Assess this cell for malaria.
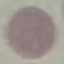
It is uninfected.

capture: smartphone through the microscope eyepiece
stain: Giemsa
image_type: automatically extracted cell patch, resized to 64 × 64 pixels
preparation: thin blood smear